Locate every blood parasite and identify its species.
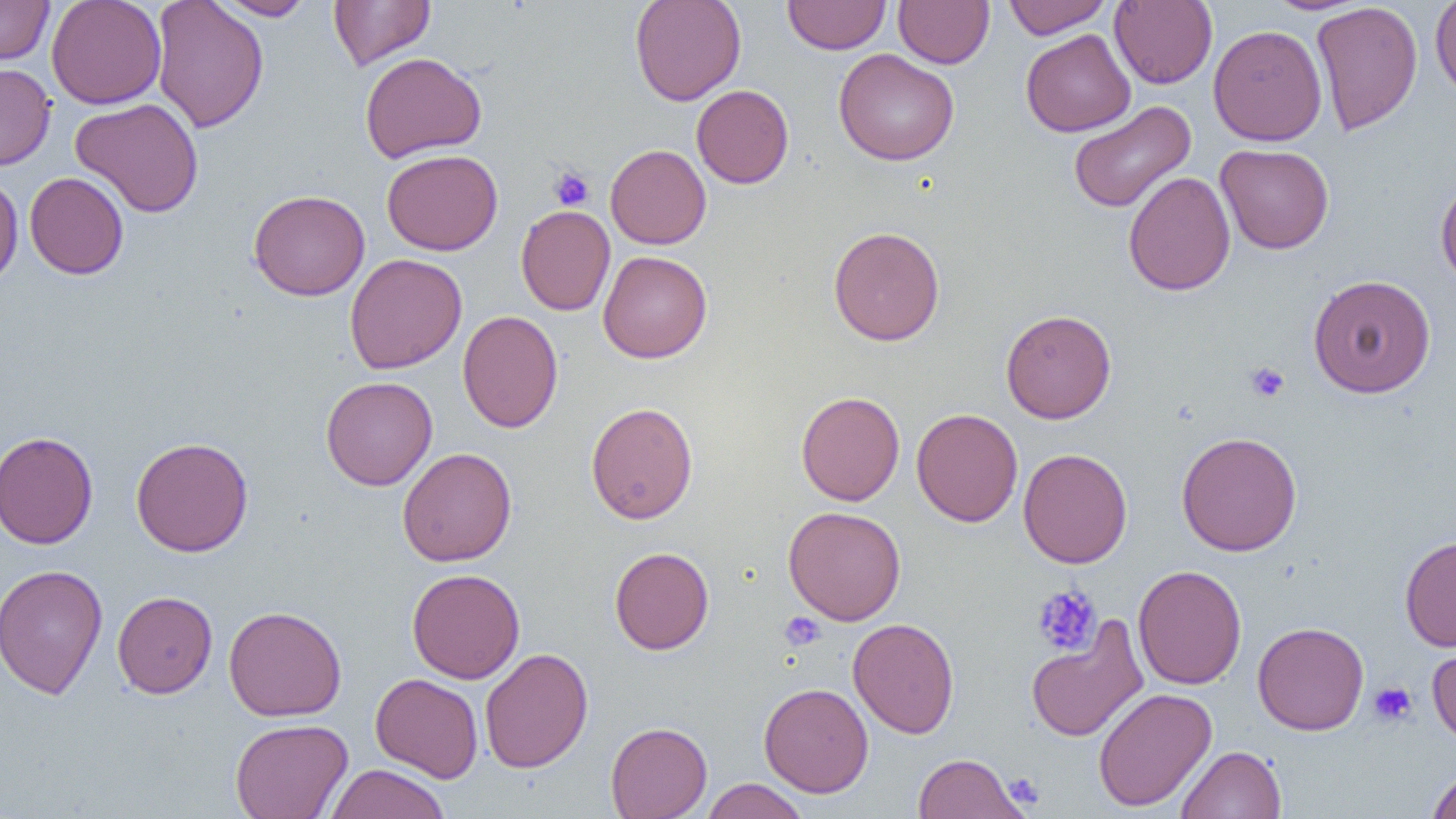
No blood parasites observed.

Summary:
  - Coordinate format: approximate bounding boxes as (x1,y1)-(x2,y2) corner pairs in pixels
  - Platelet locations: (549,167)-(595,211), (1245,362)-(1289,403), (1032,584)-(1102,656), (780,612)-(825,650), (1368,681)-(1417,726), (1003,772)-(1044,809)
  - Uninfected red blood cell locations: (0,0)-(54,65), (46,0)-(166,109), (150,0)-(269,133), (211,0)-(317,20), (328,0)-(435,71), (629,0)-(746,106), (782,0)-(890,54), (893,0)-(994,68), (1002,0)-(1111,39), (1110,0)-(1218,89), (1430,0)-(1456,102), (1310,2)-(1423,137), (1208,24)-(1327,146), (1021,29)-(1135,137), (833,48)-(959,166), (359,52)-(486,162), (0,63)-(56,171), (691,84)-(794,188), (71,98)-(204,218), (1068,101)-(1196,214), (1215,143)-(1334,254), (605,144)-(711,250), (381,149)-(503,256), (1122,171)-(1235,296), (25,172)-(128,279), (0,173)-(23,289), (1435,177)-(1456,290), (248,189)-(370,301), (516,206)-(615,315), (828,226)-(945,346), (597,250)-(712,363), (345,253)-(466,374), (1307,274)-(1436,398), (1001,309)-(1116,424), (457,310)-(563,433), (321,376)-(437,490), (796,391)-(905,506), (586,401)-(698,524), (911,408)-(1023,527), (0,431)-(99,549), (1176,431)-(1302,557), (130,436)-(254,557), (397,447)-(516,567), (1018,448)-(1132,568), (783,506)-(906,625), (1399,535)-(1456,651), (609,547)-(714,654), (0,564)-(109,699), (1133,564)-(1247,690), (407,569)-(525,683), (112,590)-(218,698), (224,605)-(347,721), (848,618)-(960,738), (1026,618)-(1148,742), (1252,621)-(1369,735), (1426,636)-(1456,748), (480,648)-(593,773), (370,673)-(483,783), (759,682)-(874,797), (1093,687)-(1217,812), (230,718)-(353,819), (605,721)-(712,818), (1177,745)-(1286,818), (914,752)-(1026,818), (324,763)-(451,819), (1427,768)-(1456,819), (700,779)-(811,819)
  - Slide-level diagnosis: negative for blood parasites
  - Modality: light microscopy
  - Field of view: one of a larger specimen
  - Preparation: thin blood film
  - Magnification: 1000x
  - Image size: 1456×819 pixels